Assess this cell for malaria.
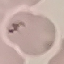
It is uninfected.

preparation = thin blood film
capture = smartphone camera at the microscope eyepiece
stain = Giemsa
image type = cell patch, automatically extracted from a larger field of view and resized to 64 × 64 pixels